Assess this cell for malaria.
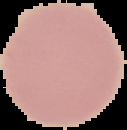
It is uninfected.

From a thin blood film. Segmented cell region on a black background. Image is 127×130 pixels.